State which parasite is depicted.
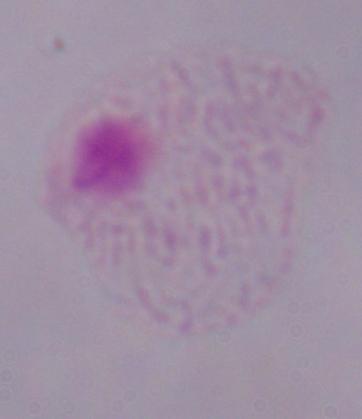
A trichomonad.

Captured at 1000x magnification. Micrograph.